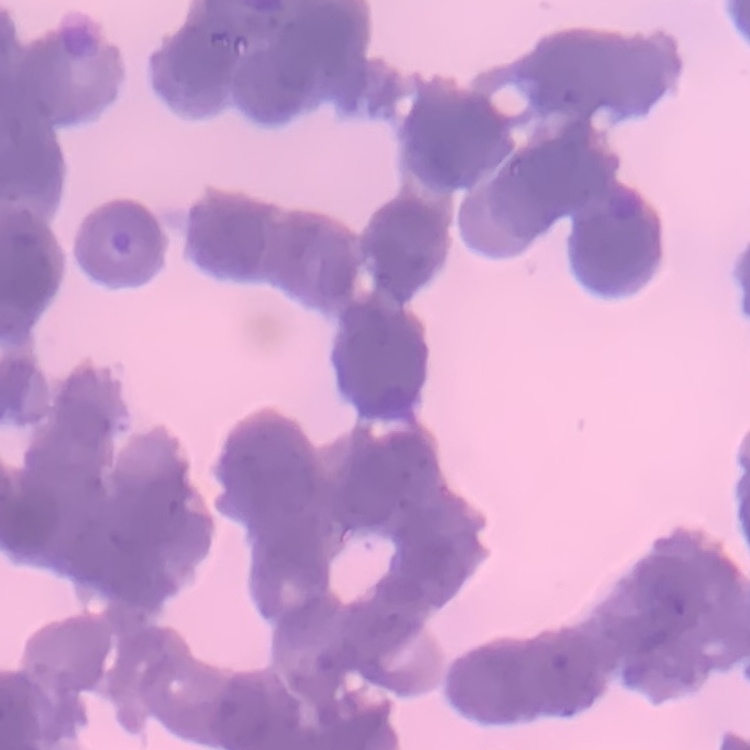 The red blood cells show rouleaux formation. Square crop of a larger photomicrograph. Thin blood smear. Field's or Giemsa stain.